Name the malaria species.
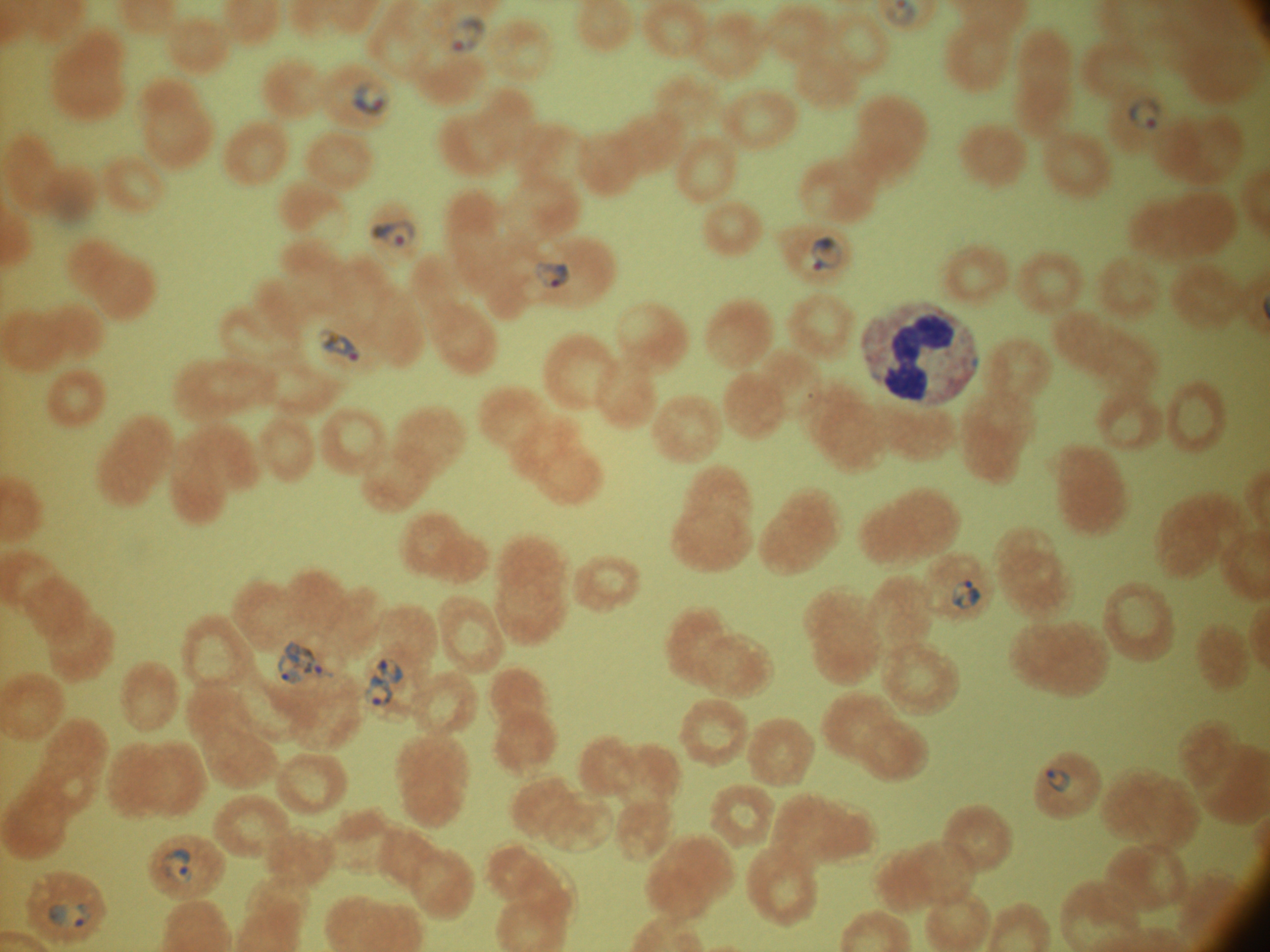
Plasmodium falciparum.

Approximate bounding boxes as named x1/y1/x2/y2 corners in pixels, from the source annotation, which is not necessarily exhaustive.
Summary:
  - Ring form locations: (x1=452, y1=16, x2=487, y2=54), (x1=352, y1=80, x2=390, y2=115), (x1=1128, y1=95, x2=1161, y2=129), (x1=370, y1=220, x2=416, y2=247), (x1=812, y1=235, x2=843, y2=271), (x1=534, y1=261, x2=571, y2=288), (x1=318, y1=328, x2=361, y2=362), (x1=950, y1=579, x2=982, y2=610), (x1=276, y1=640, x2=336, y2=687), (x1=376, y1=657, x2=404, y2=684), (x1=366, y1=673, x2=393, y2=707), (x1=1045, y1=768, x2=1071, y2=792), (x1=161, y1=847, x2=193, y2=882), (x1=48, y1=903, x2=93, y2=928)
  - Stain: Giemsa
  - Image size: 1270×952 pixels
  - Magnification: 100x
  - Field of view: single
  - Microscope: Leica DM2000 with built-in camera
  - Preparation: thin blood smear